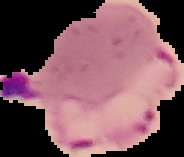

preparation: thin blood film
image_size: 184×157 pixels
malaria_status: parasitized
image_type: cell region segmented out of the field of view; surrounding area masked to black